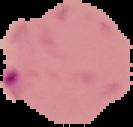

malaria status = parasitized
preparation = thin blood film
image type = cell region segmented out of the field of view; surrounding area masked to black
image size = 133×127 pixels